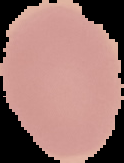

Summary:
  - Image type: cell region segmented out of the field of view; surrounding area masked to black
  - Image size: 124×163 pixels
  - Result: negative for Plasmodium parasites
  - Preparation: thin blood smear